Classify this cell by malaria status.
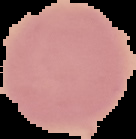

Uninfected.

From a thin blood film. Segmented cell region on a black background. Image is 136×139 pixels.